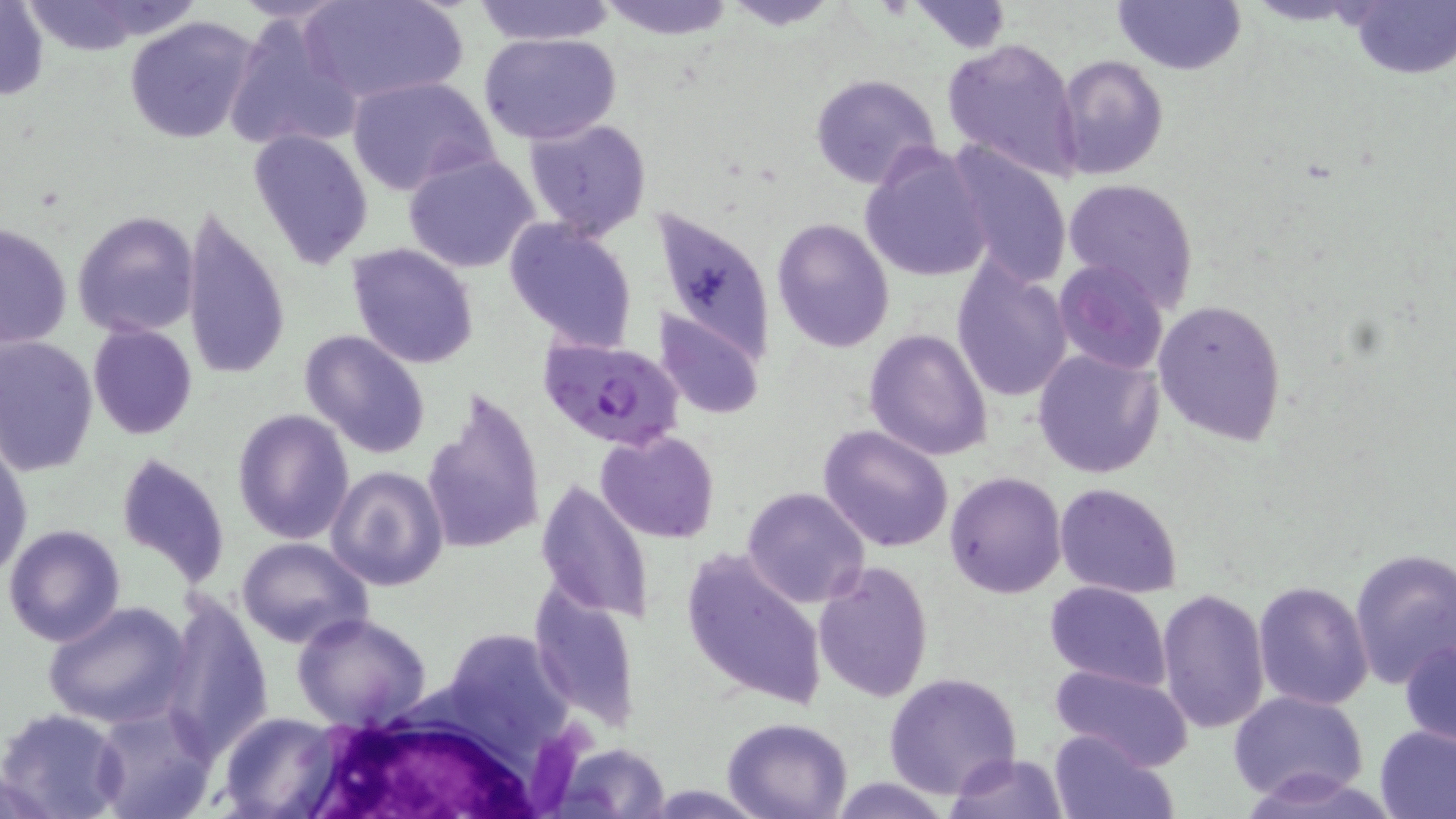

Approximate bounding boxes as [x1, y1, x2, y2] in pixels. Uninfected red blood cell locations: [302, 0, 466, 106], [471, 0, 618, 46], [594, 0, 736, 40], [720, 0, 847, 29], [907, 1, 1014, 53], [1111, 1, 1246, 76], [1344, 1, 1456, 81], [0, 2, 50, 102], [14, 2, 171, 56], [225, 12, 360, 156], [122, 16, 260, 145], [479, 31, 623, 145], [942, 36, 1081, 179], [1053, 54, 1169, 179], [809, 73, 944, 192], [347, 75, 500, 196], [525, 118, 652, 239], [248, 128, 375, 270], [859, 142, 994, 284], [946, 143, 1072, 290], [403, 153, 540, 273], [1062, 177, 1202, 311], [651, 201, 778, 368], [179, 206, 292, 383], [72, 211, 200, 338], [771, 218, 895, 353], [502, 219, 639, 352], [1, 223, 72, 349], [346, 242, 480, 368], [949, 258, 1075, 405], [1054, 260, 1170, 375], [1152, 299, 1287, 445], [655, 310, 764, 419], [87, 324, 197, 440], [864, 328, 994, 461], [299, 329, 433, 460], [0, 335, 99, 477], [1031, 347, 1165, 479], [421, 386, 547, 557], [232, 407, 355, 545], [817, 424, 954, 553], [596, 429, 720, 544], [1, 444, 32, 578], [115, 451, 231, 587], [327, 466, 448, 590], [945, 472, 1067, 598], [536, 480, 655, 625], [1054, 482, 1184, 599], [741, 486, 872, 608], [3, 523, 127, 647], [235, 537, 372, 649], [681, 546, 830, 711], [1348, 548, 1456, 692], [813, 561, 934, 703], [1252, 580, 1374, 712], [1044, 581, 1169, 692], [531, 587, 644, 730], [1156, 588, 1269, 734], [159, 594, 276, 757], [43, 600, 193, 731], [291, 611, 432, 732], [453, 630, 582, 747], [1400, 636, 1456, 748], [1049, 664, 1194, 771], [884, 672, 1023, 798], [1230, 690, 1368, 803], [92, 704, 218, 818], [0, 707, 127, 819], [218, 711, 341, 818], [723, 716, 853, 819], [1374, 723, 1456, 819], [1047, 728, 1175, 819], [555, 743, 670, 817], [945, 752, 1069, 818], [1240, 767, 1401, 818], [823, 777, 958, 817]. Plasmodium falciparum-infected red blood cell locations: [537, 335, 685, 453]. White blood cell locations: [287, 700, 578, 815]. Slide-level diagnosis: Plasmodium falciparum. Thin blood film. Image is 1456×819 pixels. Optical microscopy. 1000x magnification. Single field of view. May-Grünwald-Giemsa stain.